Report the malaria status of this cell.
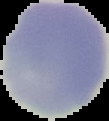
It is uninfected.

image size = 109×121 pixels
preparation = thin blood smear
image type = segmented cell region with the area outside set to black